Identify the parasite.
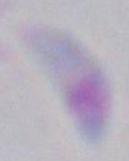
This is Toxoplasma gondii.

{
  "magnification": "1000x",
  "modality": "micrograph"
}